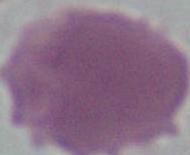
Summary:
  - Magnification: 1000x
  - Identification: red blood cell
  - Modality: micrograph